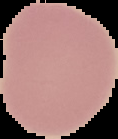
preparation = thin blood film
malaria status = uninfected
image type = segmented cell region on a black background
image size = 118×139 pixels